Describe the morphology of the red blood cells.
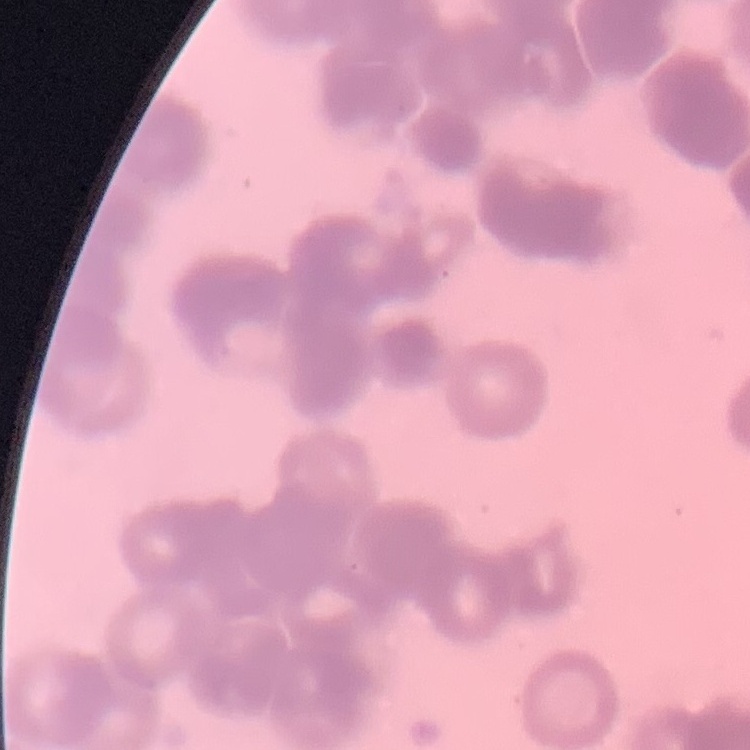

Rouleaux formation.

One tile cut from a larger photomicrograph. Thin blood smear. Field's or Giemsa stain.